Classify this cell by malaria status.
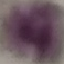

It is uninfected.

preparation = thin blood smear
image type = cell patch, automatically extracted from a larger field of view and resized to 64 × 64 pixels
capture = smartphone camera at the microscope eyepiece
stain = Giemsa